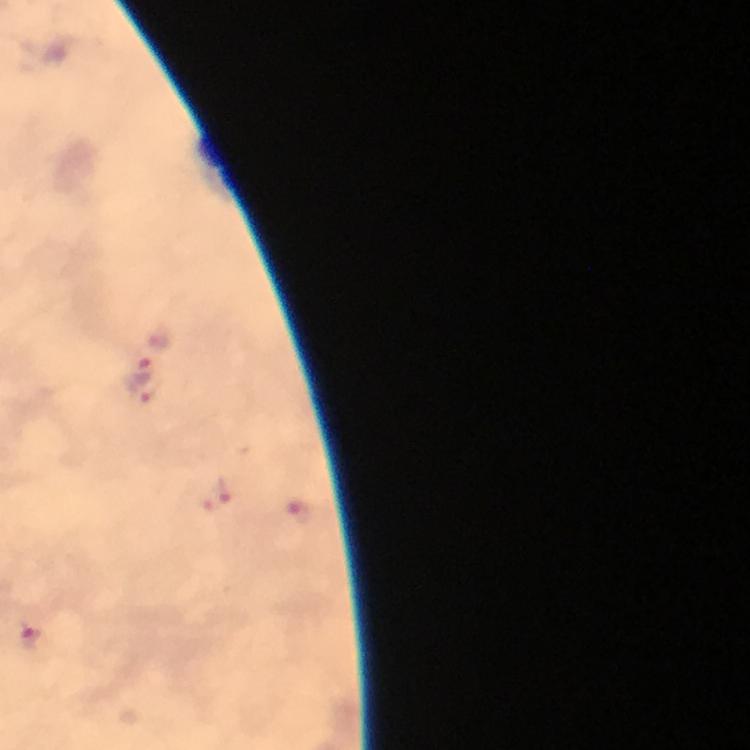 Approximate object centers, in pixels from the top-left corner. Plasmodium parasite locations: (x=155, y=348), (x=144, y=387), (x=212, y=497), (x=296, y=509), (x=30, y=637). Photographed with a smartphone mounted on the microscope. From a diagnostic examination for malaria. Thick blood film. 100x magnification. Image is 750×750 pixels. Cropped region of a single field of view. Immersion oil applied. Giemsa stain.